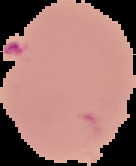
result = malaria parasites identified
preparation = thin blood film
image type = cell region segmented out of the field of view; surrounding area masked to black
image size = 136×166 pixels